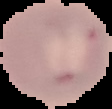

Summary:
  - Image type: segmented cell region on a black background
  - Preparation: thin blood smear
  - Image size: 112×109 pixels
  - Malaria status: uninfected